Assess this cell for malaria.
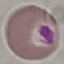

Uninfected.

image type = automatically extracted cell patch, resized to 64 × 64 pixels
stain = Giemsa
preparation = thin blood smear
capture = smartphone through the microscope eyepiece